Which red blood cells are Plasmodium falciparum-infected, and which are of indeterminate infection status?
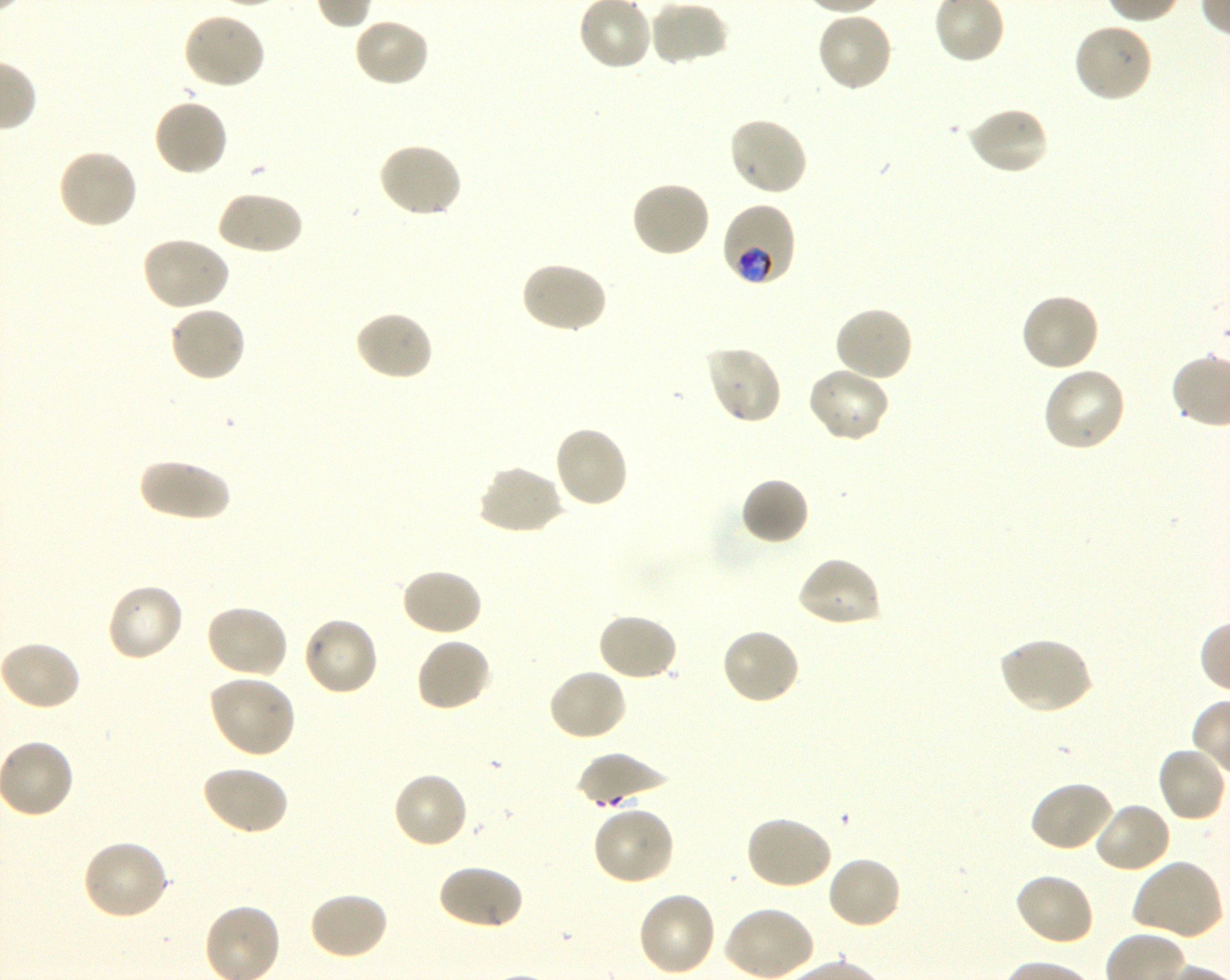
Approximate bounding rectangles given as corner coordinates in pixels from the top-left. Not every red blood cell is marked. A life-cycle stage — or a range of stages, where the recorded stages span more than one — follows each staged infected red blood cell.
Infected red blood cells: (x1=719, y1=201, x2=797, y2=288) trophozoite.
No red blood cells of indeterminate infection status observed.

Summary:
  - Locations of uninfected red blood cells: (x1=649, y1=0, x2=729, y2=67), (x1=182, y1=12, x2=265, y2=91), (x1=815, y1=12, x2=894, y2=93), (x1=352, y1=17, x2=431, y2=89), (x1=1072, y1=23, x2=1154, y2=104), (x1=152, y1=97, x2=230, y2=178), (x1=964, y1=106, x2=1049, y2=177), (x1=727, y1=115, x2=809, y2=198), (x1=376, y1=141, x2=463, y2=219), (x1=56, y1=148, x2=139, y2=231), (x1=628, y1=180, x2=711, y2=258), (x1=215, y1=190, x2=303, y2=256), (x1=140, y1=236, x2=232, y2=312), (x1=519, y1=260, x2=608, y2=335), (x1=1019, y1=291, x2=1101, y2=374), (x1=168, y1=304, x2=247, y2=383), (x1=834, y1=305, x2=914, y2=384), (x1=354, y1=310, x2=435, y2=383), (x1=703, y1=345, x2=783, y2=426), (x1=806, y1=366, x2=890, y2=444), (x1=1041, y1=366, x2=1127, y2=453), (x1=552, y1=424, x2=631, y2=509), (x1=138, y1=456, x2=231, y2=523), (x1=476, y1=464, x2=564, y2=536), (x1=739, y1=477, x2=810, y2=546), (x1=795, y1=556, x2=883, y2=629), (x1=400, y1=566, x2=483, y2=638), (x1=106, y1=582, x2=185, y2=663), (x1=204, y1=603, x2=290, y2=680), (x1=596, y1=612, x2=679, y2=683), (x1=301, y1=615, x2=379, y2=697), (x1=719, y1=627, x2=801, y2=707), (x1=415, y1=636, x2=493, y2=712), (x1=997, y1=636, x2=1094, y2=714), (x1=0, y1=640, x2=82, y2=711), (x1=547, y1=667, x2=629, y2=743), (x1=207, y1=674, x2=297, y2=759), (x1=1156, y1=744, x2=1228, y2=824), (x1=575, y1=753, x2=671, y2=807), (x1=200, y1=764, x2=290, y2=836), (x1=391, y1=770, x2=470, y2=849), (x1=1028, y1=779, x2=1115, y2=853), (x1=1093, y1=800, x2=1173, y2=874), (x1=591, y1=806, x2=675, y2=886), (x1=743, y1=815, x2=834, y2=891), (x1=81, y1=839, x2=170, y2=921), (x1=826, y1=855, x2=903, y2=931), (x1=1132, y1=858, x2=1225, y2=941), (x1=437, y1=862, x2=524, y2=931), (x1=1012, y1=871, x2=1095, y2=946), (x1=309, y1=891, x2=389, y2=961), (x1=636, y1=891, x2=718, y2=978), (x1=722, y1=905, x2=814, y2=980)
  - Stain: Giemsa
  - Image size: 1230×980 pixels
  - Culture: in-vitro Plasmodium falciparum strain 3D7, shaking
  - Objective: 100x, oil immersion, numerical aperture 1.30
  - Preparation: thin blood smear
  - Donor blood group: O+
  - Field of view: single